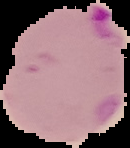
Summary:
  - Image size: 130×148 pixels
  - Image type: segmented cell region on a black background
  - Preparation: thin blood smear
  - Result: malaria parasites detected